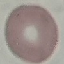 Malaria status: uninfected. Giemsa-stained preparation. Thin smear of blood. Automatically extracted cell patch, resized to 64 × 64 pixels. Acquired by smartphone through the microscope eyepiece.